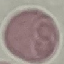
Malaria status: uninfected. Thin smear of blood. Photographed with a smartphone camera at the microscope eyepiece. Cell patch, automatically extracted from a larger field of view and resized to 64 × 64 pixels. Giemsa stain.